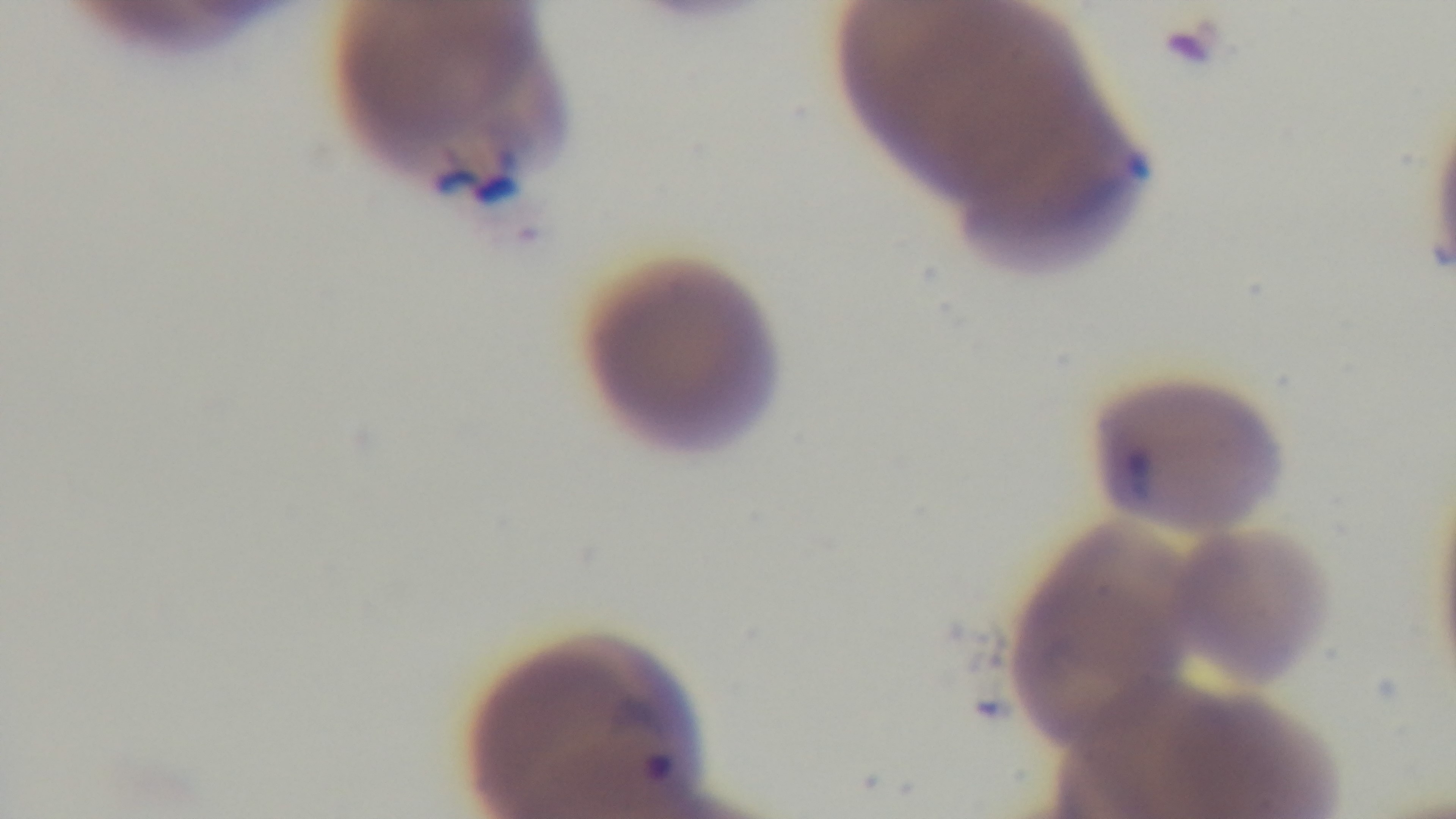 Mounted 4K digital camera. One field from the slide. Giemsa stain. Light microscopy. Malaria status: positive. Preparation: thin. Oil-immersion objective, 100x.